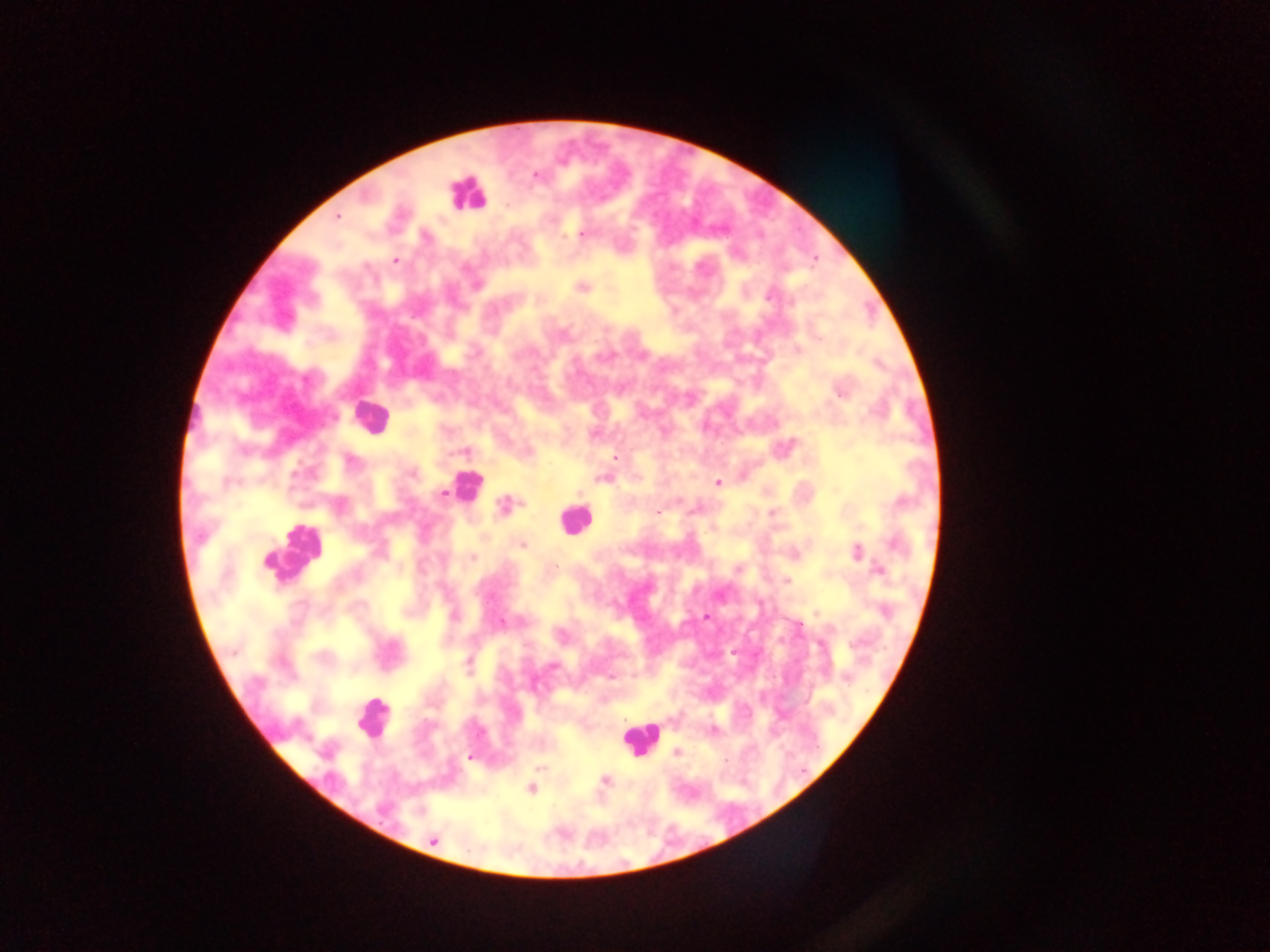

image size = 1270×952 pixels
Plasmodium parasite locations = approximate centers as {x, y} in pixels: {536, 175}, {505, 205}, {337, 216}, {582, 235}, {395, 261}, {582, 288}, {769, 297}, {797, 349}, {839, 393}, {665, 432}, {462, 452}, {614, 457}, {351, 461}, {602, 478}, {718, 482}, {443, 493}, {580, 494}, {679, 500}, {503, 505}, {658, 513}, {521, 545}, {856, 552}, {473, 558}, {556, 566}, {878, 570}, {787, 581}, {492, 598}, {816, 612}, {454, 616}, {706, 616}, {501, 623}, {733, 652}, {468, 663}, {553, 666}, {611, 676}, {712, 731}, {676, 752}, {469, 757}, {725, 760}, {540, 768}, {605, 780}, {531, 789}, {434, 841}
capture = mobile-phone photograph through a microscope
country = Ghana
preparation = thick blood film
leukocyte locations = approximate centers as {x, y} in pixels: {465, 193}, {368, 416}, {466, 486}, {575, 521}, {292, 551}, {372, 718}, {640, 739}
field of view = single